Locate every Plasmodium ovale-infected red blood cell.
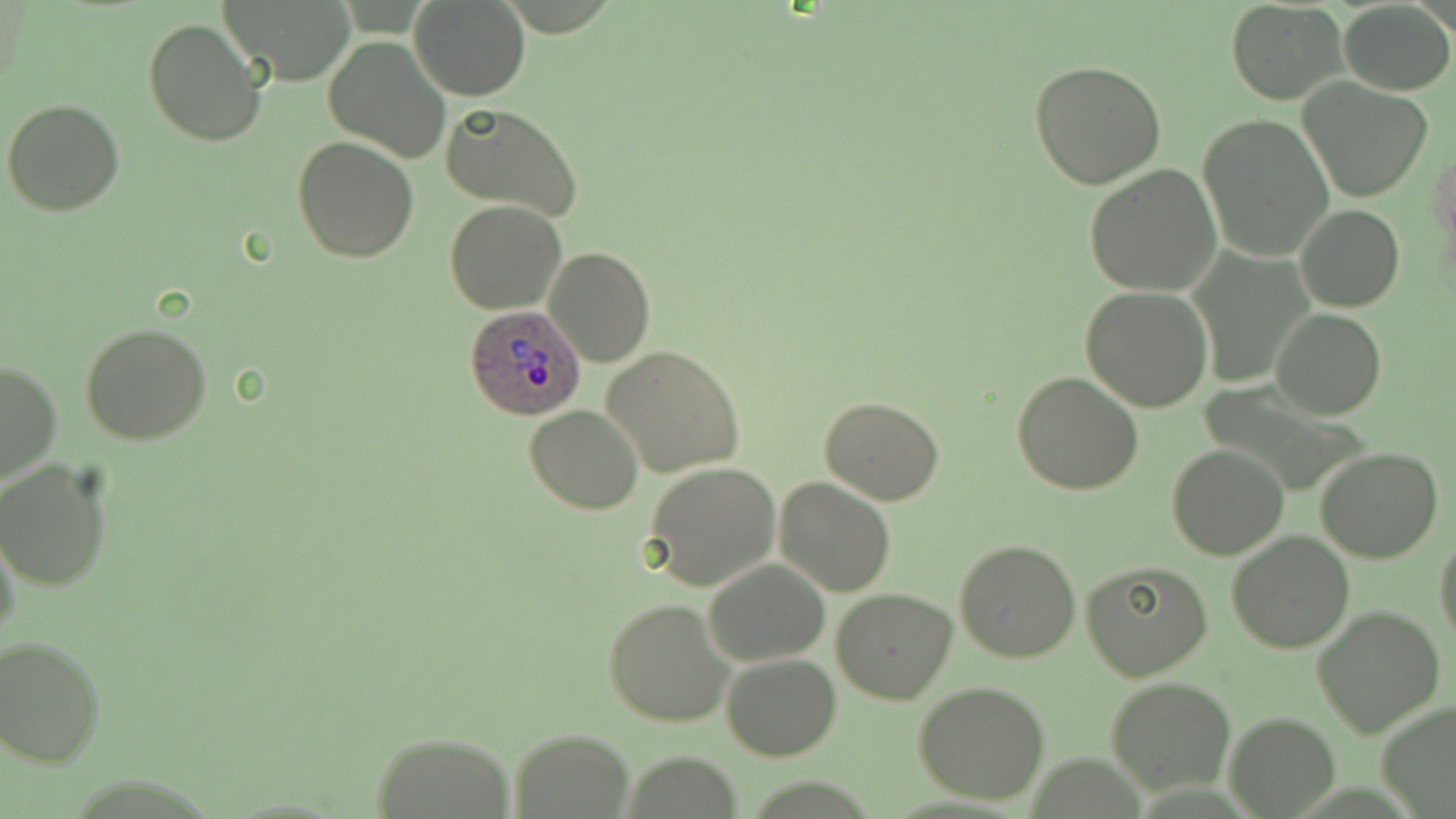
Approximate bounding boxes as (x1, y1, x2, y2) in pixels.
Plasmodium ovale-infected red blood cells: (463, 304, 586, 421).

Uninfected red blood cell locations: (214, 0, 357, 84), (409, 0, 528, 100), (1226, 0, 1347, 104), (1338, 2, 1455, 95), (142, 17, 269, 147), (322, 36, 451, 164), (1029, 59, 1169, 190), (1299, 79, 1432, 202), (4, 99, 126, 218), (439, 102, 585, 224), (1199, 113, 1334, 262), (291, 137, 419, 262), (1082, 164, 1222, 298), (444, 201, 566, 315), (1295, 205, 1405, 313), (544, 246, 655, 367), (1081, 287, 1213, 411), (1272, 309, 1386, 419), (79, 322, 212, 446), (602, 345, 745, 477), (1, 358, 63, 490), (1013, 370, 1143, 494), (820, 396, 946, 506), (525, 405, 643, 514), (1168, 445, 1290, 561), (1314, 447, 1444, 564), (0, 459, 115, 591), (643, 462, 781, 590), (774, 478, 896, 597), (0, 527, 23, 649), (1226, 530, 1355, 653), (1433, 531, 1456, 649), (952, 539, 1081, 663), (704, 558, 829, 666), (1081, 560, 1212, 680), (831, 587, 958, 705), (604, 596, 734, 727), (1311, 605, 1446, 739), (0, 635, 104, 768), (722, 652, 840, 760), (1106, 676, 1237, 796), (913, 681, 1052, 805), (1374, 701, 1456, 817), (1225, 711, 1339, 817), (510, 727, 633, 816), (368, 732, 518, 818). Slide-level diagnosis: Plasmodium ovale. Single field of view. Thin blood film. Image is 1456×819 pixels. May-Grünwald-Giemsa-stained preparation. Light microscopy. Captured at 1000x magnification.